State the blood parasite species.
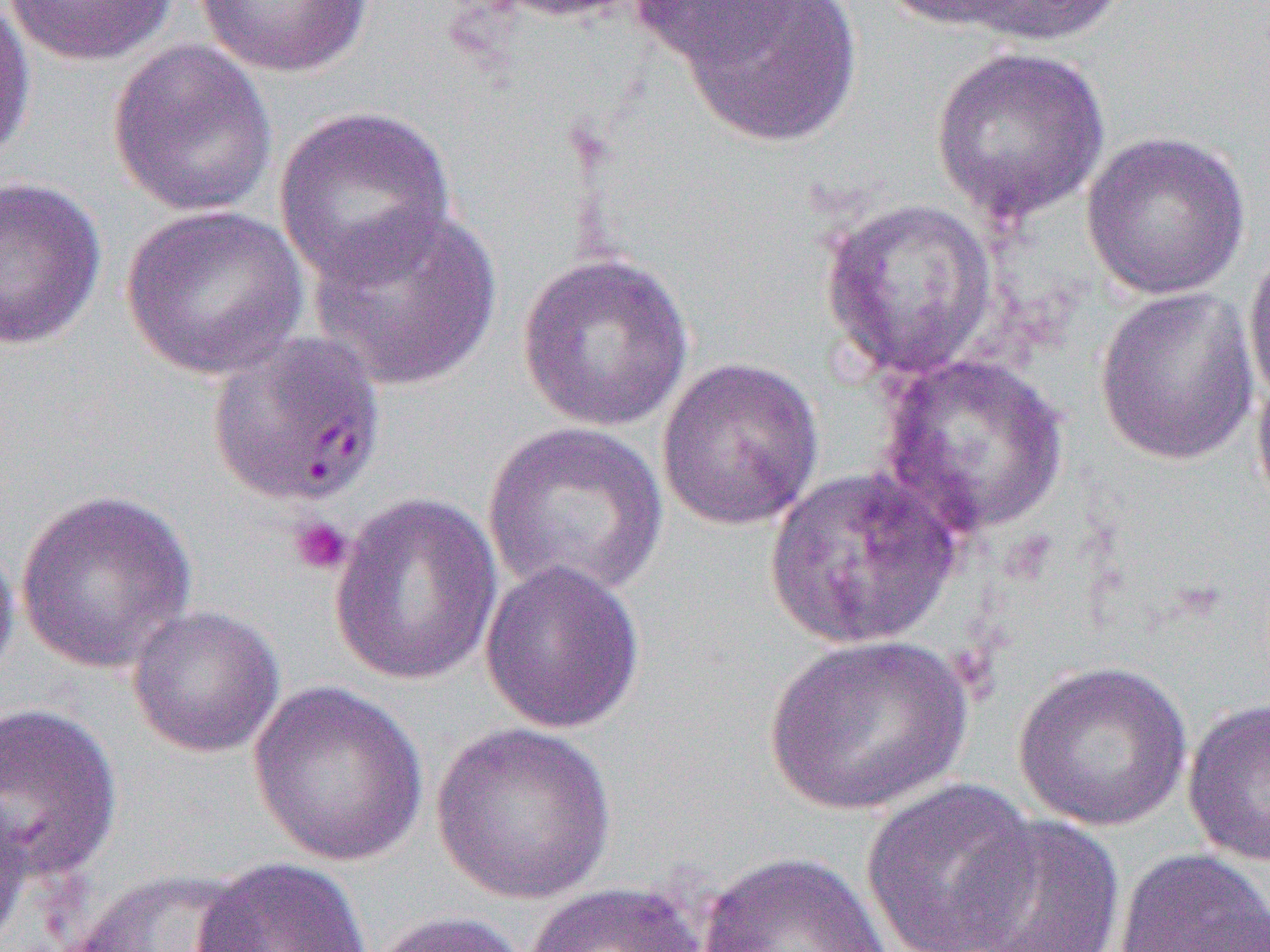
Plasmodium falciparum.

Summary:
  - Coordinate format: approximate bounding boxes as [x1, y1, x2, y2] in pixels
  - Platelet locations: [288, 515, 353, 576]
  - Uninfected red blood cell locations: [2, 0, 180, 66], [192, 0, 375, 78], [476, 0, 650, 23], [873, 0, 1038, 33], [940, 0, 1129, 49], [0, 1, 36, 166], [623, 1, 814, 72], [674, 1, 865, 148], [107, 40, 278, 220], [929, 45, 1110, 223], [273, 105, 457, 286], [1080, 131, 1251, 300], [0, 175, 107, 352], [818, 196, 999, 382], [306, 203, 504, 392], [120, 205, 310, 381], [1242, 237, 1270, 409], [517, 251, 695, 432], [1094, 286, 1259, 466], [878, 351, 1070, 539], [655, 357, 825, 531], [1250, 357, 1270, 521], [483, 421, 669, 601], [763, 465, 964, 651], [15, 488, 197, 674], [329, 491, 504, 686], [0, 532, 21, 689], [479, 559, 647, 735], [126, 604, 285, 758], [762, 633, 975, 817], [1013, 659, 1193, 833], [248, 680, 429, 866], [1181, 696, 1270, 867], [0, 702, 124, 882], [430, 722, 617, 905], [860, 778, 1040, 952], [0, 787, 33, 947], [955, 814, 1126, 952], [1113, 847, 1270, 952], [695, 850, 893, 952], [193, 855, 374, 952], [65, 867, 263, 951], [522, 881, 708, 952], [368, 910, 533, 952]
  - Plasmodium falciparum-infected red blood cell locations: [206, 330, 386, 508]
  - Field of view: one of a larger specimen
  - Magnification: 1000x
  - Preparation: thin blood film
  - Modality: optical microscopy
  - Image size: 1270×952 pixels